Outline each blood parasite and name the species.
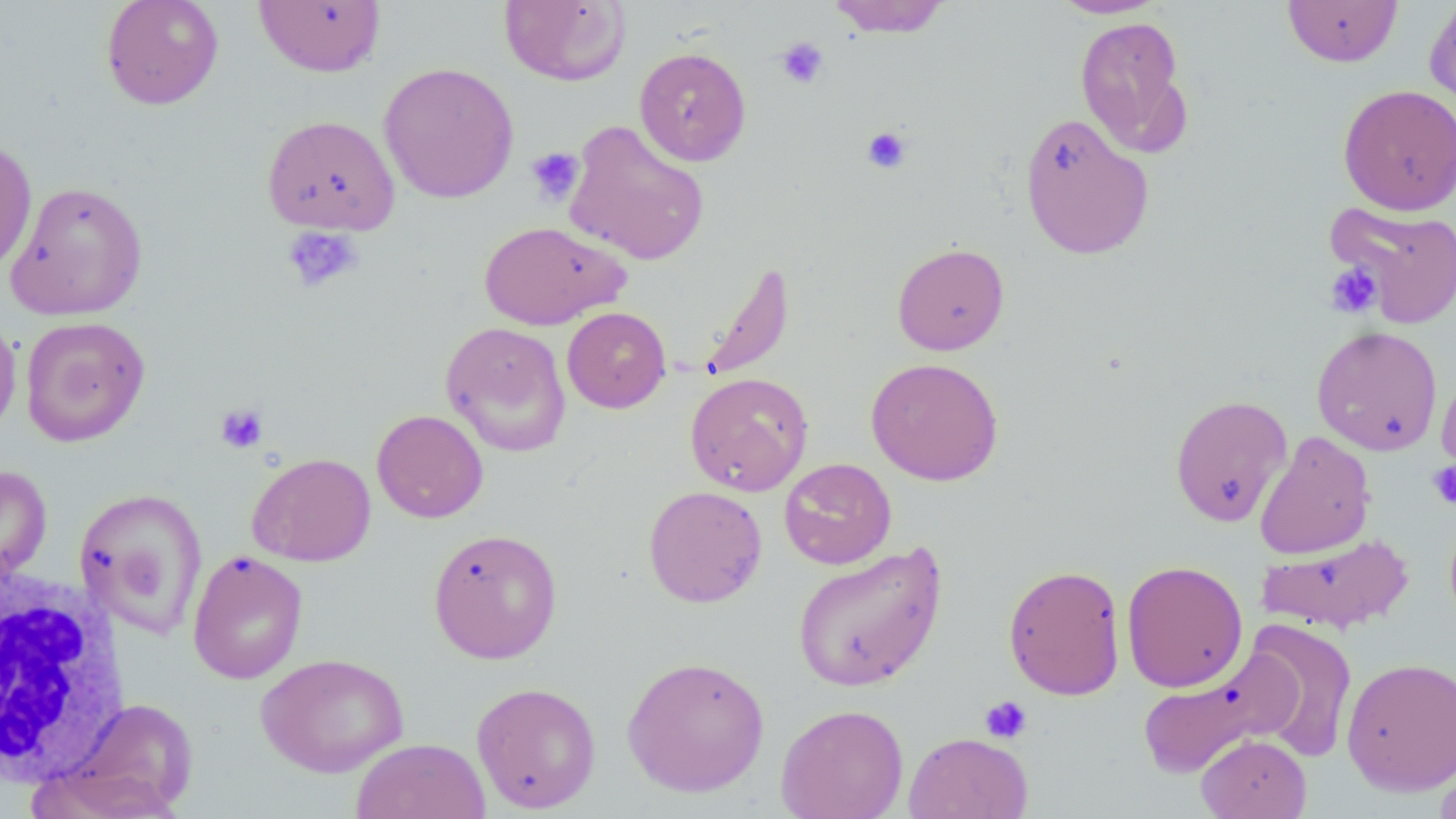

No blood parasites seen.

Approximate bounding boxes as [x1, y1, x2, y2] in pixels. White blood cell locations: [1, 562, 129, 789]. Uninfected red blood cell locations: [100, 0, 224, 110], [499, 0, 631, 87], [825, 0, 952, 38], [1048, 0, 1167, 19], [1282, 0, 1403, 67], [1424, 0, 1456, 115], [253, 1, 386, 77], [1074, 15, 1191, 156], [633, 46, 751, 166], [379, 62, 520, 204], [1339, 83, 1456, 216], [1018, 113, 1155, 261], [261, 114, 400, 235], [563, 119, 710, 266], [0, 138, 37, 275], [6, 180, 149, 321], [1324, 200, 1456, 328], [479, 221, 628, 330], [891, 242, 1010, 355], [698, 259, 795, 382], [562, 307, 671, 413], [0, 308, 21, 441], [20, 316, 150, 446], [441, 321, 572, 457], [1312, 324, 1443, 456], [866, 357, 1004, 485], [1435, 363, 1456, 487], [684, 371, 814, 496], [1170, 394, 1292, 527], [371, 408, 488, 523], [1254, 431, 1376, 559], [247, 452, 376, 567], [779, 457, 896, 570], [0, 464, 52, 585], [643, 485, 767, 607], [75, 487, 209, 638], [427, 527, 563, 664], [1256, 533, 1415, 634], [792, 542, 947, 692], [187, 550, 308, 684], [1121, 560, 1248, 693], [1003, 564, 1126, 700], [1241, 620, 1358, 763], [1136, 648, 1302, 780], [255, 652, 410, 778], [621, 655, 771, 798], [1341, 657, 1456, 794], [471, 681, 601, 813], [63, 697, 199, 815], [775, 703, 909, 819], [903, 731, 1033, 819], [1195, 733, 1312, 819], [351, 738, 490, 819], [1434, 752, 1456, 819], [24, 763, 183, 819]. Platelet locations: [775, 37, 829, 89], [862, 126, 912, 174], [525, 146, 585, 205], [282, 226, 364, 294], [1325, 263, 1383, 318], [215, 404, 269, 454], [1427, 461, 1456, 509], [980, 695, 1033, 744]. Slide-level diagnosis: negative for blood parasites. Light microscopy. 1000x magnification. One field of a larger specimen. Thin blood smear. Image is 1456×819 pixels. May-Grünwald-Giemsa-stained preparation.